State which parasite is depicted.
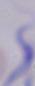
This is a trypanosome.

modality = photomicrograph
magnification = 1000x